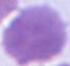 Micrograph. A red blood cell is shown. Captured at 1000x magnification.